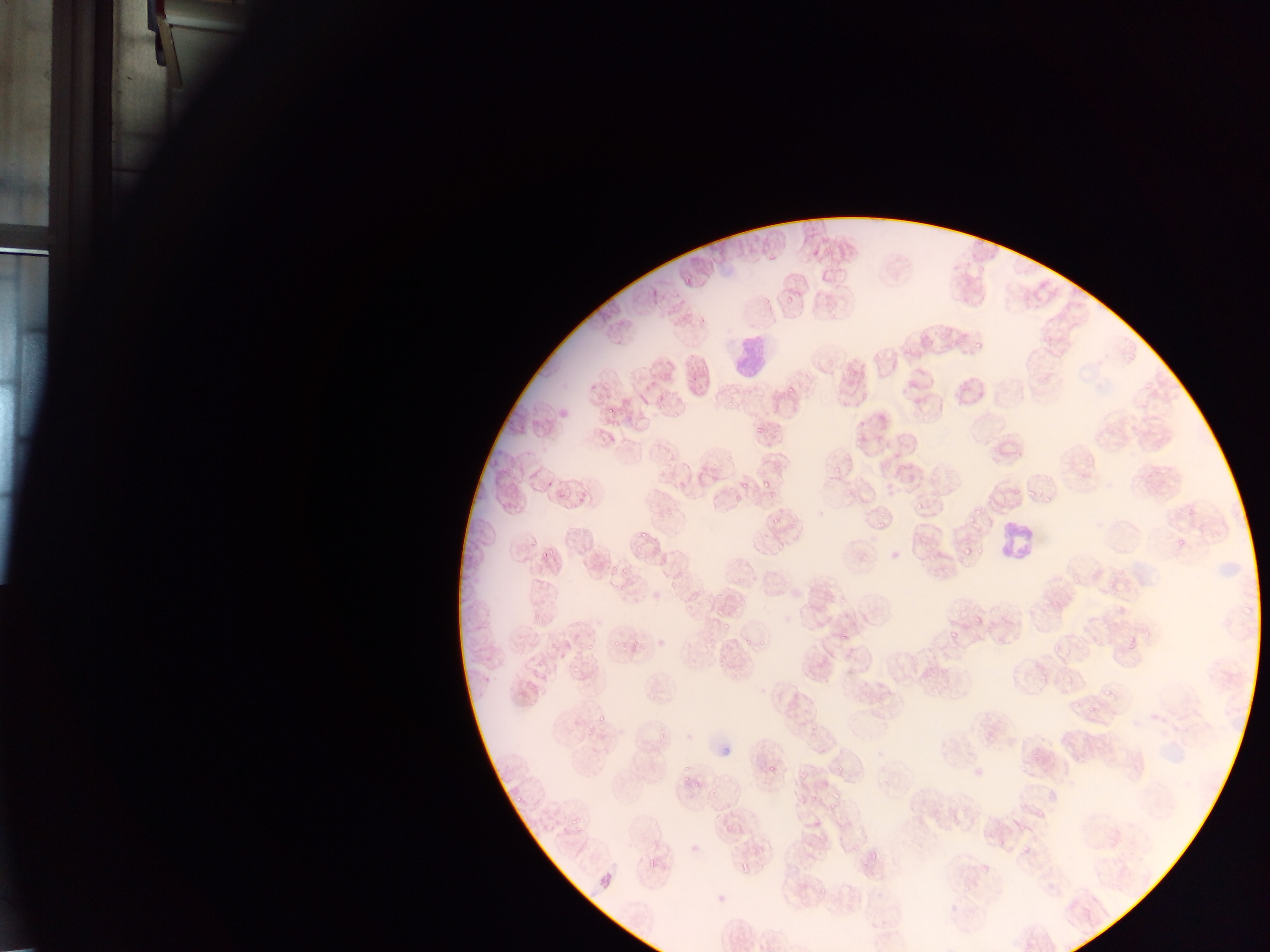 Approximate bounding boxes as {left, top, right, bottom} in pixels. Leukocyte locations: {732, 341, 770, 373}, {987, 511, 1051, 566}. Malaria parasite locations: {766, 252, 776, 260}, {790, 273, 801, 280}, {787, 292, 795, 301}, {1024, 296, 1037, 308}, {809, 303, 820, 311}, {696, 311, 709, 324}, {826, 311, 836, 319}, {1041, 332, 1053, 344}, {977, 340, 986, 348}, {902, 343, 913, 352}, {827, 359, 835, 365}, {844, 361, 858, 374}, {803, 368, 815, 383}, {701, 376, 717, 392}, {1144, 379, 1151, 390}, {784, 381, 798, 396}, {596, 390, 607, 397}, {727, 395, 739, 408}, {1140, 397, 1152, 406}, {658, 404, 668, 412}, {670, 405, 690, 418}, {608, 406, 617, 415}, {1107, 417, 1119, 430}, {756, 424, 764, 437}, {855, 435, 865, 441}, {662, 439, 673, 451}, {989, 439, 1006, 456}, {723, 448, 735, 460}, {832, 461, 839, 477}, {897, 464, 905, 473}, {544, 474, 560, 488}, {1079, 474, 1087, 479}, {659, 475, 668, 484}, {761, 478, 770, 493}, {813, 480, 835, 490}, {677, 482, 687, 489}, {738, 482, 750, 491}, {1004, 487, 1022, 498}, {1027, 487, 1037, 497}, {763, 490, 777, 501}, {554, 492, 567, 502}, {732, 493, 743, 501}, {567, 494, 587, 511}, {1041, 495, 1050, 505}, {703, 500, 715, 507}, {662, 501, 680, 516}, {912, 504, 923, 517}, {971, 504, 982, 515}, {877, 509, 889, 515}, {769, 516, 780, 525}, {966, 517, 971, 525}, {876, 519, 889, 531}, {788, 521, 800, 531}, {637, 527, 653, 538}, {568, 528, 583, 545}, {529, 532, 542, 551}, {1173, 536, 1188, 550}, {633, 539, 644, 552}, {918, 539, 927, 550}, {586, 542, 596, 551}, {975, 544, 982, 556}, {774, 545, 784, 553}, {962, 545, 970, 554}, {541, 547, 559, 563}, {929, 554, 942, 564}, {963, 560, 972, 569}, {604, 564, 618, 577}, {621, 566, 632, 575}, {736, 573, 753, 587}, {1071, 573, 1084, 584}, {1107, 575, 1124, 594}, {667, 576, 681, 589}, {630, 577, 643, 596}, {614, 583, 625, 595}, {1050, 583, 1068, 600}, {681, 588, 699, 607}, {709, 593, 723, 604}, {970, 599, 976, 610}, {711, 605, 724, 616}, {956, 606, 965, 617}, {992, 607, 1001, 614}, {528, 609, 545, 621}, {1003, 611, 1012, 620}, {944, 612, 955, 625}, {970, 615, 981, 623}, {718, 620, 732, 632}, {1123, 626, 1141, 658}, {837, 628, 851, 644}, {949, 628, 959, 639}, {1010, 629, 1019, 638}, {741, 636, 750, 645}, {1052, 638, 1063, 652}, {584, 639, 600, 652}, {757, 639, 765, 649}, {613, 640, 621, 652}, {631, 642, 640, 650}, {715, 647, 731, 668}, {643, 652, 650, 661}, {527, 656, 550, 671}, {570, 663, 586, 675}, {1040, 674, 1049, 681}, {1063, 674, 1074, 686}, {1103, 682, 1116, 706}, {642, 692, 654, 702}, {1070, 693, 1083, 707}, {527, 695, 538, 705}, {1085, 703, 1097, 715}, {594, 712, 610, 726}, {795, 717, 805, 729}, {582, 729, 595, 738}, {658, 734, 668, 745}, {595, 735, 606, 743}, {815, 745, 827, 755}, {1019, 758, 1034, 776}, {767, 760, 785, 776}, {836, 761, 849, 773}, {799, 771, 809, 780}, {879, 774, 893, 785}, {681, 775, 688, 783}, {693, 778, 701, 789}, {707, 788, 716, 800}, {515, 793, 527, 806}, {785, 797, 797, 806}, {809, 797, 817, 806}, {828, 799, 845, 810}, {961, 801, 973, 811}, {1016, 801, 1030, 812}, {713, 807, 727, 824}, {930, 811, 946, 823}, {1036, 811, 1046, 820}, {571, 815, 584, 830}, {969, 816, 982, 825}, {951, 820, 959, 827}, {996, 821, 1005, 829}, {725, 824, 736, 833}, {997, 837, 1006, 848}, {1019, 840, 1036, 853}, {690, 843, 699, 853}, {851, 844, 863, 855}, {868, 848, 881, 863}, {646, 861, 655, 873}, {981, 862, 994, 872}, {740, 865, 747, 874}, {959, 882, 973, 893}, {814, 885, 826, 899} | approximate {x, y} pixel centers of objects too small to bound: {687, 767}, {761, 869}. Collected in Ghana. Image is 1270×952 pixels. Thin blood film. Photographed through a microscope with a mobile-phone camera. Single field of view.